Classify this cell by malaria status.
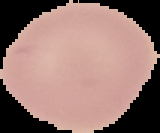
Uninfected.

Segmented cell region on a black background. From a thin blood film. Image is 160×133 pixels.